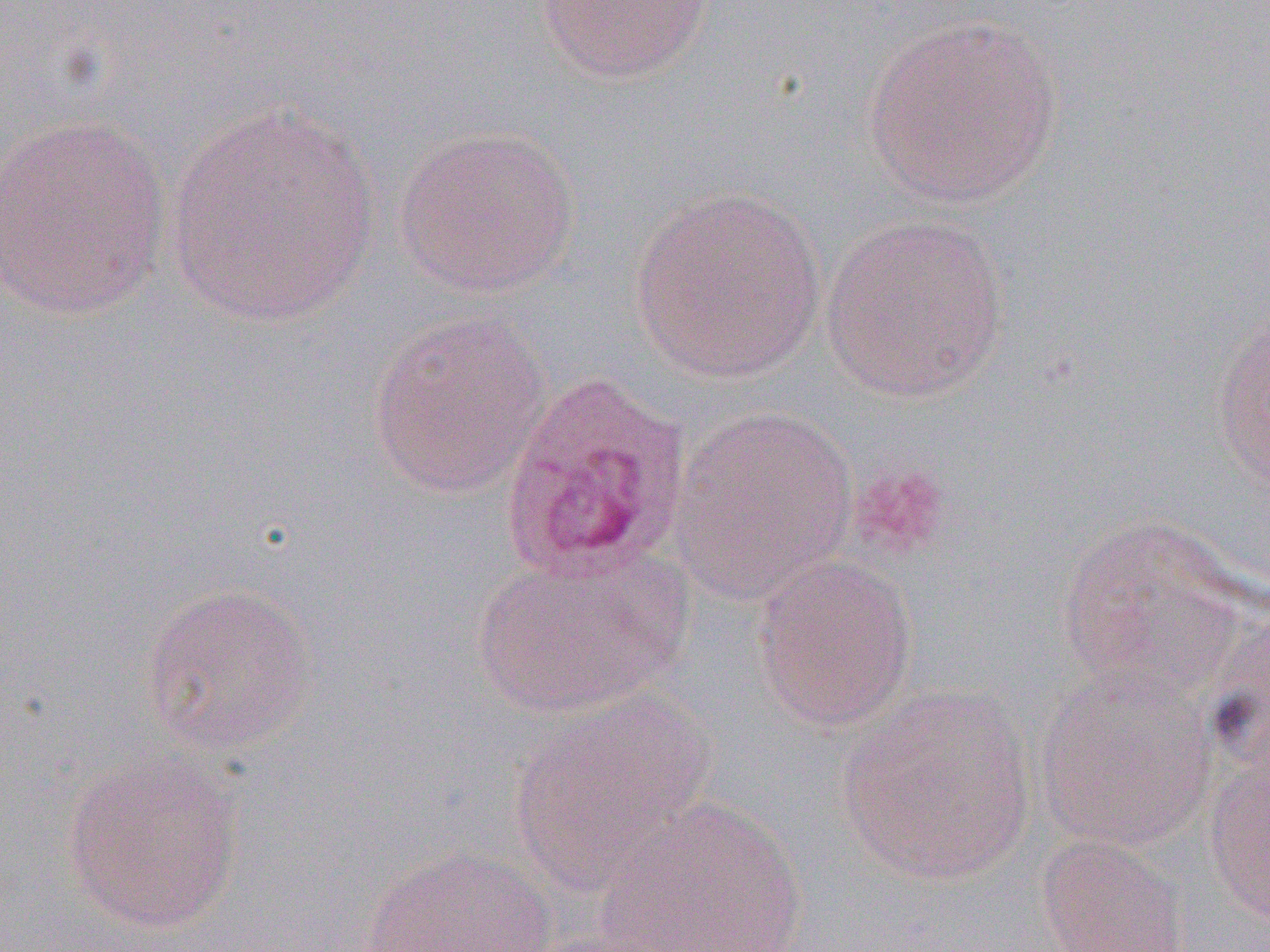

Summary:
  - Coordinate format: approximate bounding boxes as (x1,y1)-(x2,y2) corner pairs in pixels
  - Uninfected red blood cell locations: (535,0)-(715,84), (862,15)-(1063,210), (164,100)-(384,329), (0,113)-(173,322), (392,125)-(581,298), (628,187)-(828,384), (820,212)-(1012,404), (1210,304)-(1269,501), (366,310)-(552,500), (669,406)-(859,603), (1056,516)-(1252,698), (472,549)-(687,720), (751,554)-(919,732), (139,581)-(317,756), (1032,664)-(1218,852), (837,684)-(1038,886), (508,693)-(716,892), (1204,744)-(1270,925), (61,747)-(247,936), (593,795)-(810,952), (1037,835)-(1190,952), (361,846)-(557,951)
  - Platelet locations: (847,461)-(951,563)
  - Slide-level diagnosis: Plasmodium ovale
  - Image size: 1270×952 pixels
  - Preparation: thin blood film
  - Magnification: 1000x
  - Field of view: single
  - Modality: light microscopy